Outline each blood parasite and name the species.
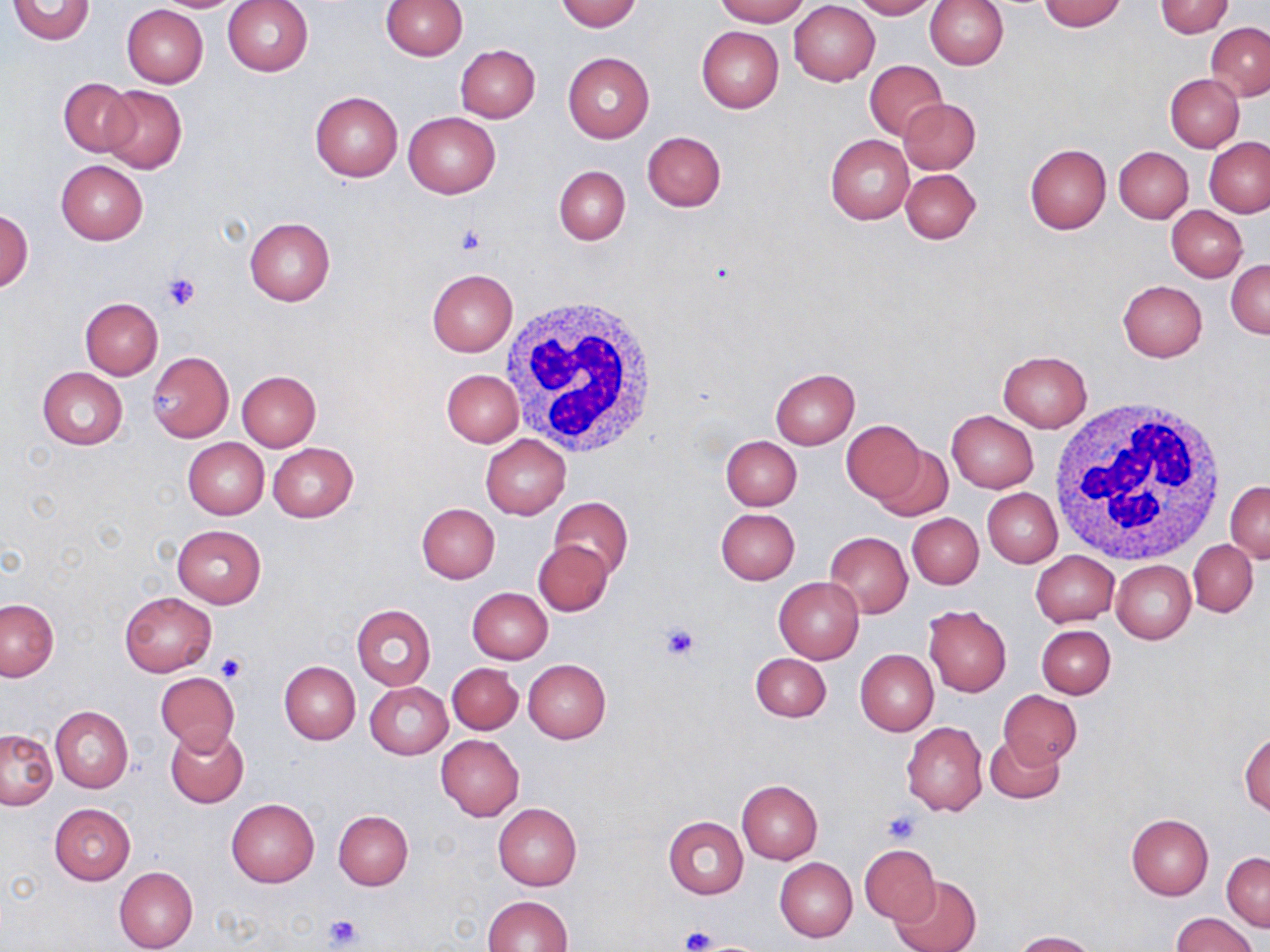
No blood parasites seen.

{
  "slide_level_diagnosis": "negative for blood parasites",
  "image_size": "1270×952 pixels",
  "uninfected_red_blood_cell_locations": "approximate bounding boxes as named x1/y1/x2/y2 corners in pixels: (x1=150, y1=0, x2=246, y2=12), (x1=222, y1=0, x2=314, y2=77), (x1=382, y1=0, x2=467, y2=60), (x1=556, y1=0, x2=641, y2=32), (x1=714, y1=0, x2=808, y2=26), (x1=851, y1=0, x2=937, y2=19), (x1=923, y1=0, x2=1008, y2=70), (x1=1038, y1=0, x2=1126, y2=31), (x1=7, y1=1, x2=96, y2=44), (x1=789, y1=1, x2=880, y2=85), (x1=1154, y1=1, x2=1234, y2=37), (x1=121, y1=4, x2=207, y2=88), (x1=1206, y1=23, x2=1269, y2=99), (x1=696, y1=26, x2=784, y2=112), (x1=454, y1=44, x2=539, y2=123), (x1=562, y1=51, x2=654, y2=143), (x1=865, y1=59, x2=947, y2=141), (x1=1165, y1=75, x2=1243, y2=152), (x1=58, y1=78, x2=139, y2=156), (x1=100, y1=83, x2=187, y2=174), (x1=309, y1=89, x2=403, y2=182), (x1=898, y1=98, x2=981, y2=175), (x1=403, y1=111, x2=500, y2=197), (x1=642, y1=131, x2=726, y2=212), (x1=825, y1=135, x2=913, y2=224), (x1=1190, y1=137, x2=1262, y2=277), (x1=1205, y1=139, x2=1270, y2=216), (x1=1025, y1=144, x2=1112, y2=234), (x1=1114, y1=146, x2=1193, y2=222), (x1=56, y1=159, x2=148, y2=244), (x1=554, y1=165, x2=631, y2=245), (x1=901, y1=168, x2=981, y2=244), (x1=1167, y1=205, x2=1248, y2=281), (x1=0, y1=209, x2=33, y2=292), (x1=245, y1=217, x2=334, y2=306), (x1=1227, y1=259, x2=1270, y2=336), (x1=427, y1=269, x2=517, y2=356), (x1=1118, y1=280, x2=1207, y2=361), (x1=80, y1=297, x2=162, y2=378), (x1=997, y1=351, x2=1091, y2=432), (x1=147, y1=352, x2=233, y2=441), (x1=38, y1=367, x2=128, y2=449), (x1=769, y1=368, x2=859, y2=448), (x1=440, y1=369, x2=523, y2=446), (x1=235, y1=370, x2=321, y2=450), (x1=946, y1=410, x2=1038, y2=492), (x1=841, y1=420, x2=926, y2=503), (x1=480, y1=434, x2=571, y2=518), (x1=720, y1=435, x2=801, y2=510), (x1=183, y1=438, x2=268, y2=520), (x1=268, y1=442, x2=359, y2=522), (x1=872, y1=443, x2=953, y2=520), (x1=1226, y1=481, x2=1270, y2=562), (x1=983, y1=489, x2=1062, y2=567), (x1=549, y1=497, x2=633, y2=580), (x1=416, y1=503, x2=499, y2=583), (x1=717, y1=508, x2=800, y2=584), (x1=908, y1=514, x2=984, y2=589), (x1=171, y1=525, x2=267, y2=607), (x1=825, y1=531, x2=912, y2=617), (x1=533, y1=539, x2=612, y2=616), (x1=1189, y1=540, x2=1257, y2=615), (x1=1031, y1=551, x2=1119, y2=626), (x1=1111, y1=560, x2=1195, y2=643), (x1=774, y1=578, x2=865, y2=664), (x1=467, y1=587, x2=553, y2=664), (x1=119, y1=592, x2=215, y2=675), (x1=0, y1=598, x2=58, y2=683), (x1=352, y1=604, x2=436, y2=690), (x1=924, y1=605, x2=1012, y2=696), (x1=1036, y1=625, x2=1115, y2=698), (x1=855, y1=649, x2=939, y2=736), (x1=750, y1=653, x2=830, y2=722), (x1=280, y1=660, x2=360, y2=744), (x1=524, y1=660, x2=611, y2=742), (x1=447, y1=662, x2=522, y2=734), (x1=154, y1=672, x2=240, y2=753), (x1=365, y1=682, x2=452, y2=759), (x1=997, y1=689, x2=1082, y2=768), (x1=50, y1=706, x2=133, y2=793), (x1=902, y1=721, x2=987, y2=816), (x1=165, y1=726, x2=249, y2=806), (x1=1, y1=729, x2=57, y2=810), (x1=1239, y1=730, x2=1269, y2=815), (x1=436, y1=734, x2=524, y2=820), (x1=985, y1=734, x2=1063, y2=804), (x1=737, y1=780, x2=822, y2=863), (x1=226, y1=798, x2=319, y2=886), (x1=50, y1=804, x2=135, y2=884), (x1=493, y1=804, x2=581, y2=890), (x1=334, y1=811, x2=413, y2=890), (x1=1125, y1=813, x2=1214, y2=899), (x1=663, y1=815, x2=748, y2=899), (x1=859, y1=844, x2=941, y2=925), (x1=1222, y1=852, x2=1269, y2=930), (x1=774, y1=857, x2=857, y2=942), (x1=114, y1=866, x2=198, y2=952), (x1=891, y1=876, x2=981, y2=952), (x1=482, y1=896, x2=572, y2=952), (x1=1171, y1=913, x2=1259, y2=952), (x1=1012, y1=930, x2=1097, y2=952)",
  "preparation": "thin blood smear",
  "white_blood_cell_locations": "approximate bounding boxes as named x1/y1/x2/y2 corners in pixels: (x1=498, y1=295, x2=660, y2=457), (x1=1049, y1=397, x2=1228, y2=568)",
  "magnification": "1000x",
  "stain": "May-Grünwald-Giemsa",
  "platelet_locations": "approximate bounding boxes as named x1/y1/x2/y2 corners in pixels: (x1=457, y1=224, x2=488, y2=257), (x1=162, y1=272, x2=202, y2=312), (x1=658, y1=622, x2=700, y2=663), (x1=218, y1=653, x2=246, y2=682), (x1=882, y1=809, x2=923, y2=844), (x1=324, y1=914, x2=363, y2=950), (x1=680, y1=925, x2=715, y2=951)",
  "field_of_view": "one of a larger specimen",
  "modality": "light microscopy"
}